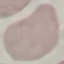
Result: negative for malaria parasites. Acquired by smartphone through the microscope eyepiece. Thin blood film. Giemsa stain. Automatically extracted cell patch, resized to 64 × 64 pixels.